Report the malaria status of this cell.
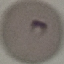
Parasitized.

{
  "image_type": "automatically extracted cell patch, resized to 64 × 64 pixels",
  "stain": "Giemsa",
  "capture": "smartphone camera at the microscope eyepiece",
  "preparation": "thin smear"
}